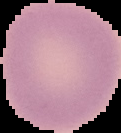

Summary:
  - Malaria status: uninfected
  - Image type: cell region segmented out of the field of view; surrounding area masked to black
  - Image size: 121×133 pixels
  - Preparation: thin blood smear